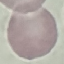
Result: no malaria parasites detected. Thin blood film. Automatically extracted cell patch, resized to 64 × 64 pixels. Giemsa stain. Photographed with a smartphone camera at the microscope eyepiece.